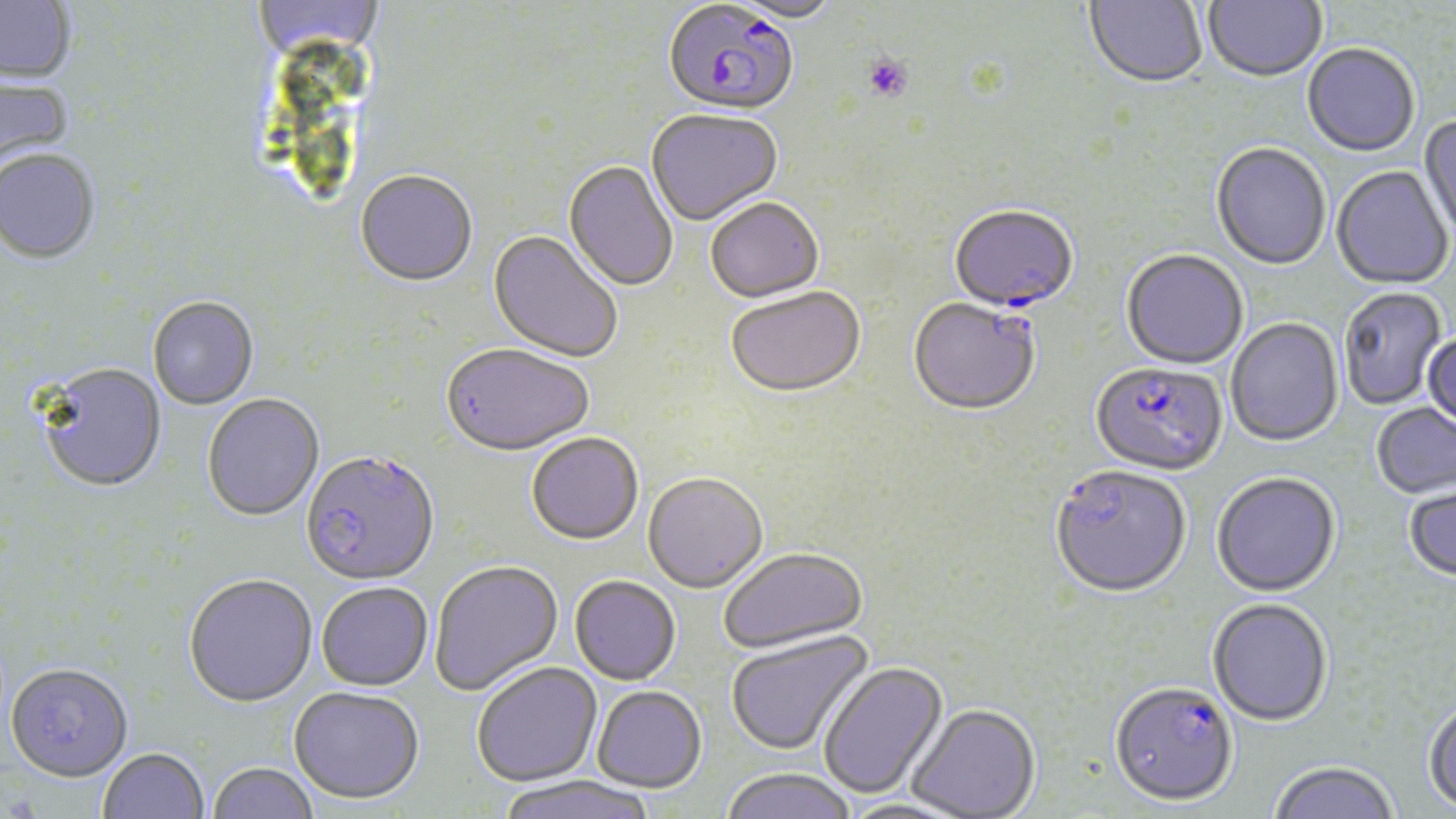
Summary:
  - Coordinate format: approximate bounding boxes as (x1,y1)-(x2,y2) corner pairs in pixels
  - Plasmodium falciparum-infected red blood cell locations: (662,4)-(799,119), (948,207)-(1079,316), (911,294)-(1043,412), (1090,363)-(1228,479), (301,451)-(440,587), (1050,467)-(1192,601), (1109,684)-(1239,809)
  - Platelet locations: (862,54)-(912,102)
  - Uninfected red blood cell locations: (0,0)-(76,84), (254,0)-(384,62), (727,0)-(842,26), (1084,0)-(1207,91), (1203,0)-(1327,85), (1302,45)-(1420,159), (0,75)-(75,177), (646,110)-(784,228), (1418,114)-(1456,246), (1210,144)-(1331,272), (0,152)-(100,265), (563,161)-(678,293), (1331,167)-(1454,291), (355,172)-(478,289), (705,200)-(825,305), (487,230)-(622,365), (1121,251)-(1248,371), (726,288)-(866,401), (1339,288)-(1447,411), (148,297)-(259,410), (1226,318)-(1344,449), (1422,333)-(1456,435), (440,345)-(594,458), (38,363)-(167,493), (202,394)-(325,521), (1371,403)-(1455,501), (527,434)-(645,547), (643,474)-(767,594), (1212,475)-(1341,599), (1403,483)-(1456,586), (718,548)-(868,655), (429,561)-(563,696), (184,574)-(317,707), (569,576)-(681,686), (316,583)-(434,692), (1207,600)-(1333,729), (726,630)-(875,757), (473,662)-(602,786), (5,663)-(133,783), (819,663)-(949,800), (592,686)-(707,793), (289,688)-(424,806), (1423,700)-(1456,815), (907,706)-(1041,819), (98,749)-(209,819), (207,762)-(319,819), (1269,763)-(1400,819), (720,769)-(857,819), (494,776)-(658,819)
  - Slide-level diagnosis: Plasmodium falciparum
  - Magnification: 1000x
  - Modality: optical microscopy
  - Image size: 1456×819 pixels
  - Stain: May-Grünwald-Giemsa
  - Field of view: one of a larger specimen
  - Preparation: thin blood smear